Name the parasite shown.
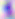
This is Toxoplasma gondii.

Photomicrograph. Captured at 400x magnification.